Comment on the morphology of the red blood cells.
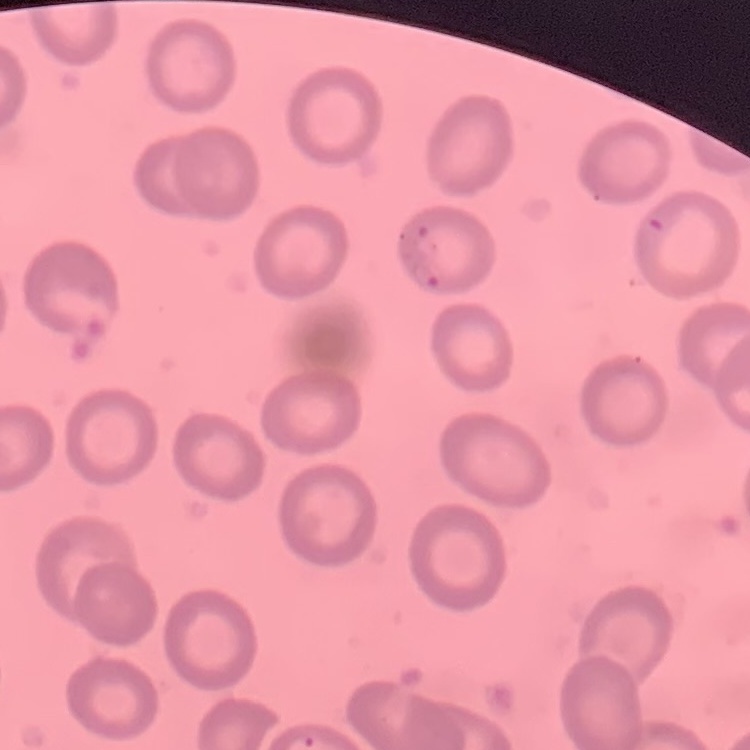
They show no rouleaux formation.

Thin blood smear. One tile cut from a larger photomicrograph. Stained with either Field's or Giemsa.